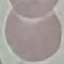
Summary:
  - Malaria status: uninfected
  - Capture: smartphone camera at the microscope eyepiece
  - Stain: Giemsa
  - Preparation: thin smear
  - Image type: automatically extracted cell patch, resized to 64 × 64 pixels